State which parasite is depicted.
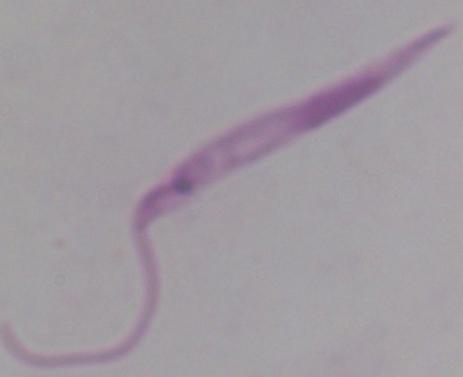

This is Leishmania.

Micrograph. 1000x magnification.